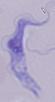

{
  "modality": "photomicrograph",
  "magnification": "1000x",
  "identification": "trypanosome"
}